Assess this cell for malaria.
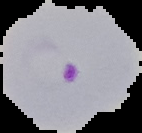
It is parasitized.

{
  "preparation": "thin blood film",
  "image_type": "segmented cell region on a black background",
  "image_size": "142×133 pixels"
}